Report the malaria status.
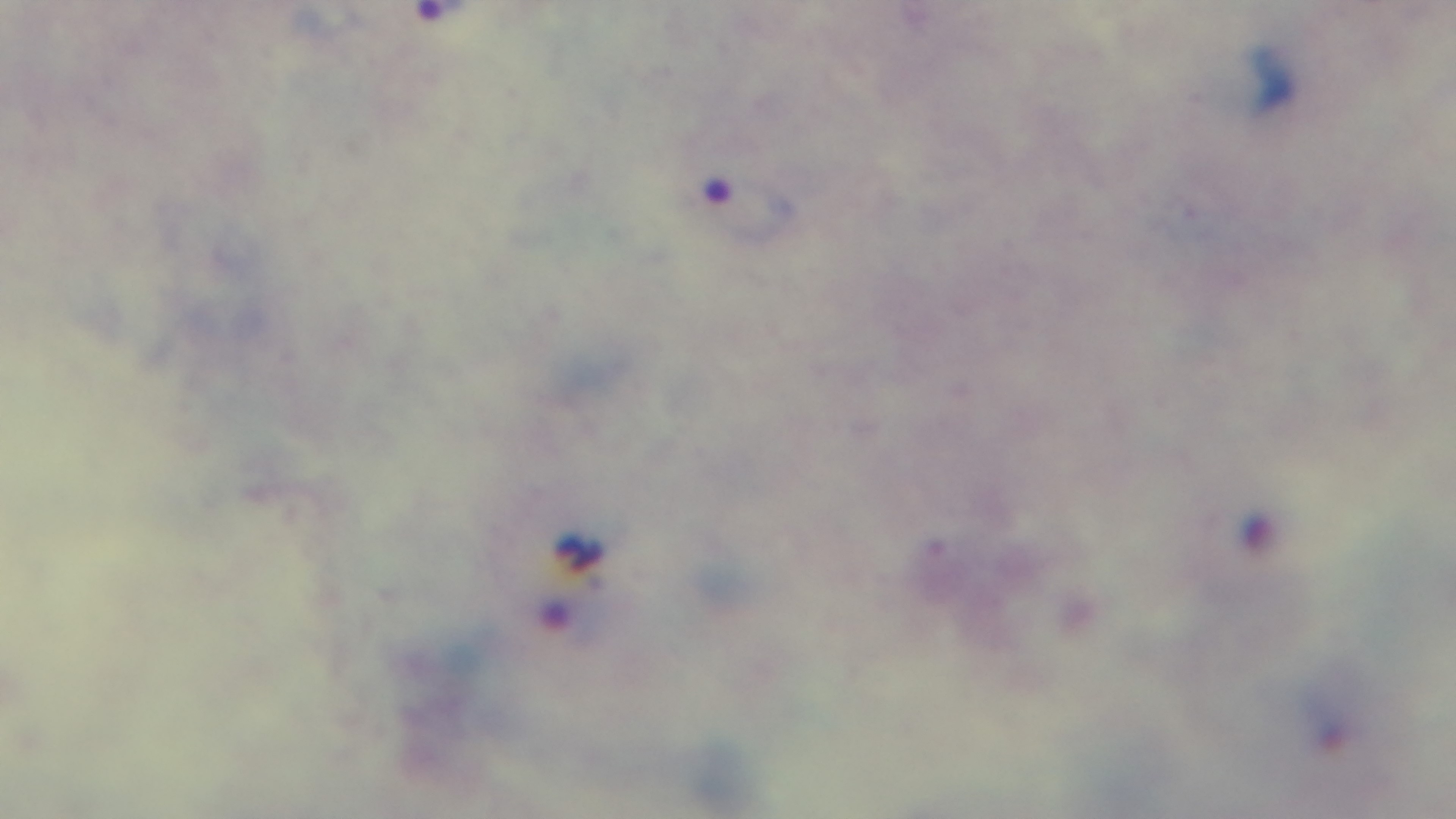
Positive.

Summary:
  - Preparation: thick
  - Capture: mounted 4K digital camera
  - Stain: Giemsa
  - Objective: 100x oil immersion
  - Field of view: one from the slide
  - Modality: light microscopy